Assess the morphology of the erythrocytes.
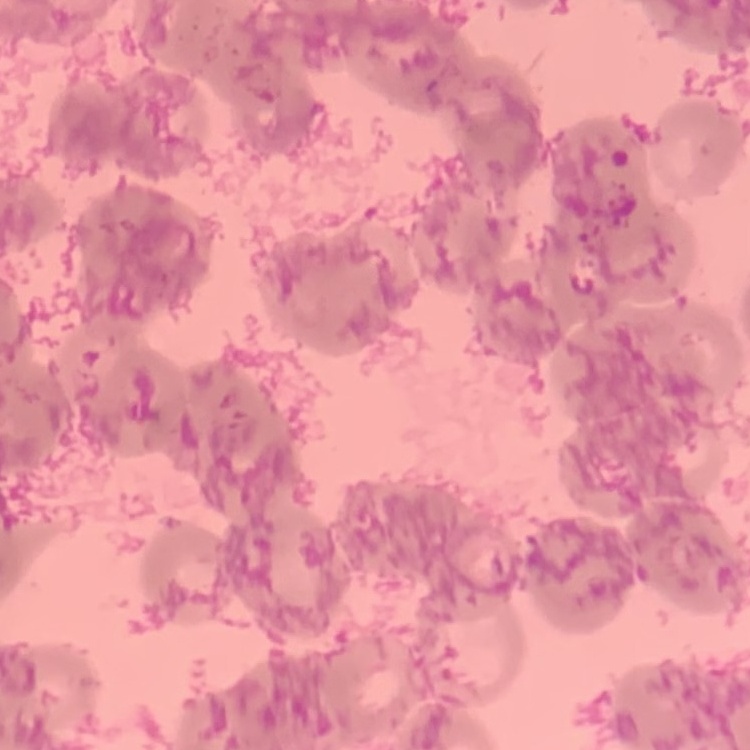

Rouleaux formation.

Summary:
  - Stain: Field's or Giemsa
  - Preparation: thin blood film
  - Image type: one tile cut from a larger photomicrograph